Identify the parasite.
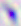

Toxoplasma gondii.

Captured at 400x magnification. Micrograph.